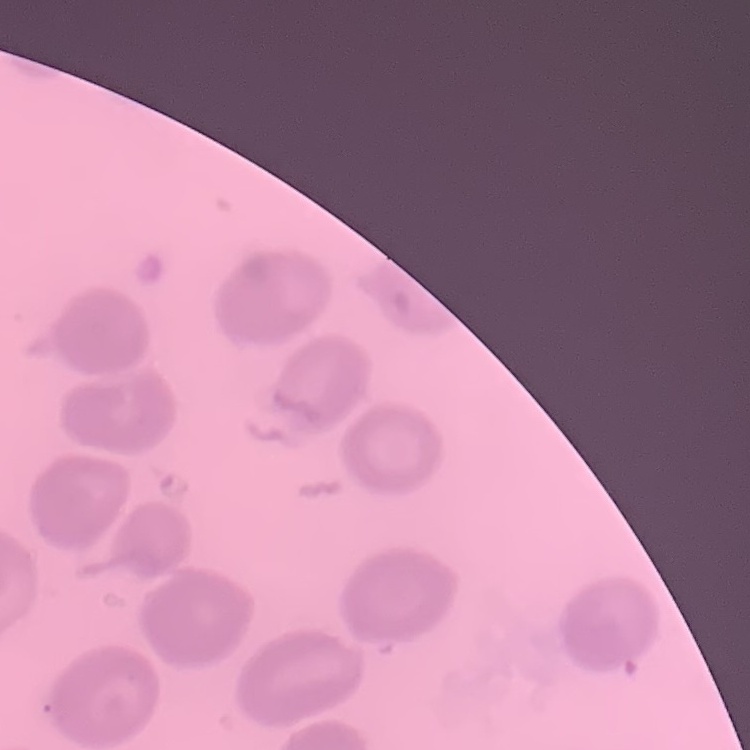 The erythrocytes exhibit no rouleaux formation. Thin blood smear. One tile cut from a larger photomicrograph. Field's or Giemsa stain.